Name the parasite shown.
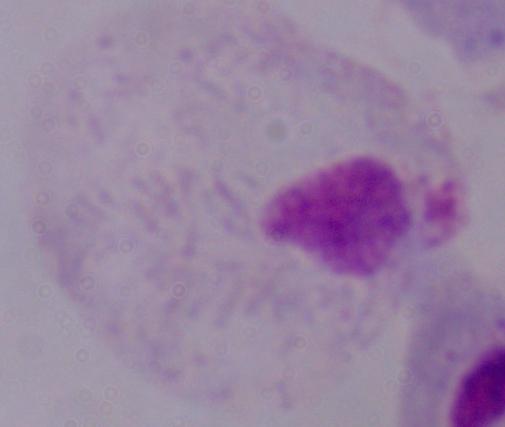

This is a trichomonad.

Summary:
  - Magnification: 1000x
  - Modality: micrograph